Identify the preparation type.
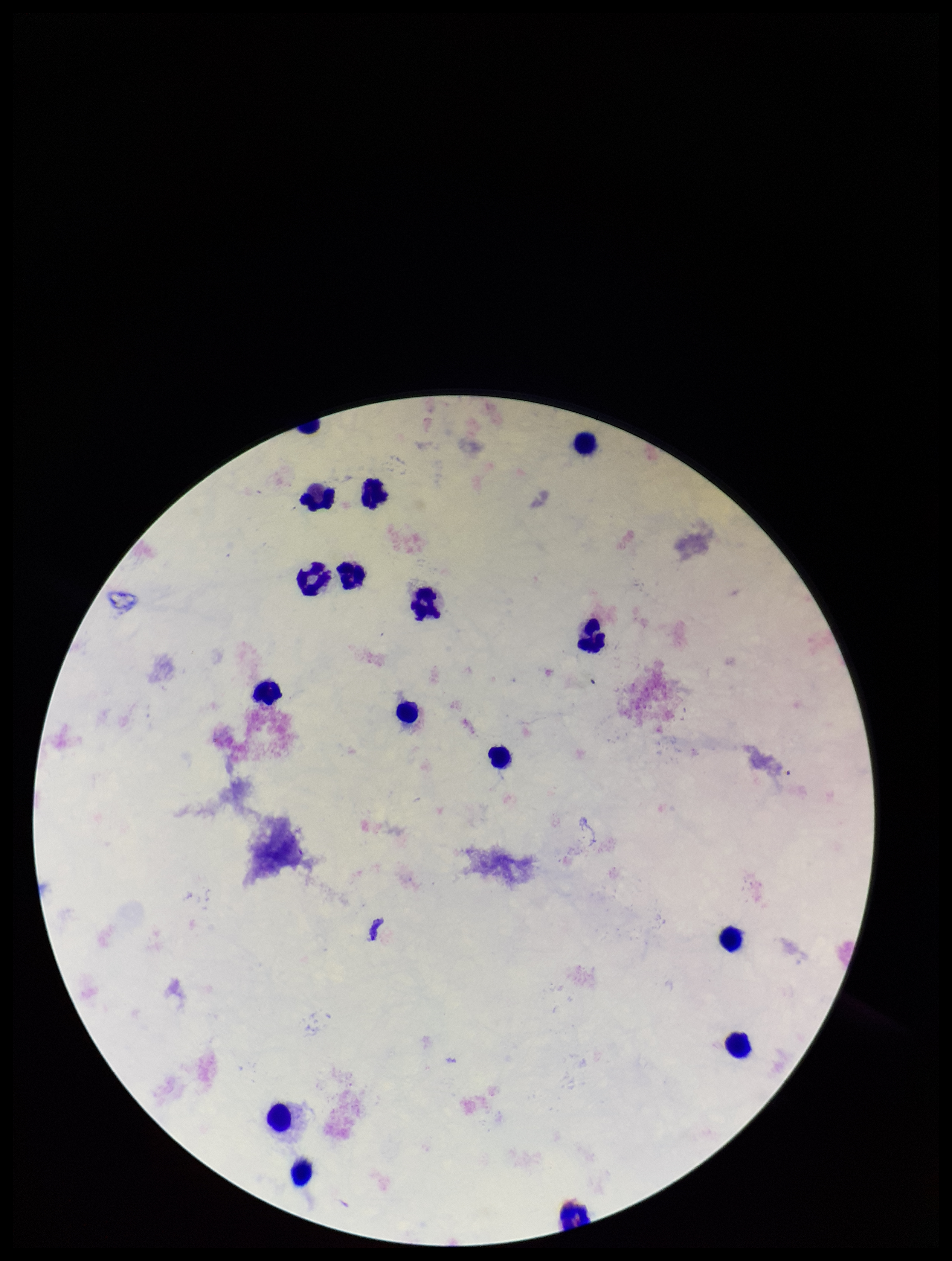

Thick.

{
  "parasite_count": 0,
  "field_of_view": "single",
  "patient_malaria_status": "negative",
  "capture": "smartphone photograph through the microscope eyepiece",
  "stain": "Giemsa",
  "leukocyte_count": 15,
  "image_size": "952×1261 pixels",
  "plasmodium_parasites": "none identified"
}